Give the position of every leukocyte visible.
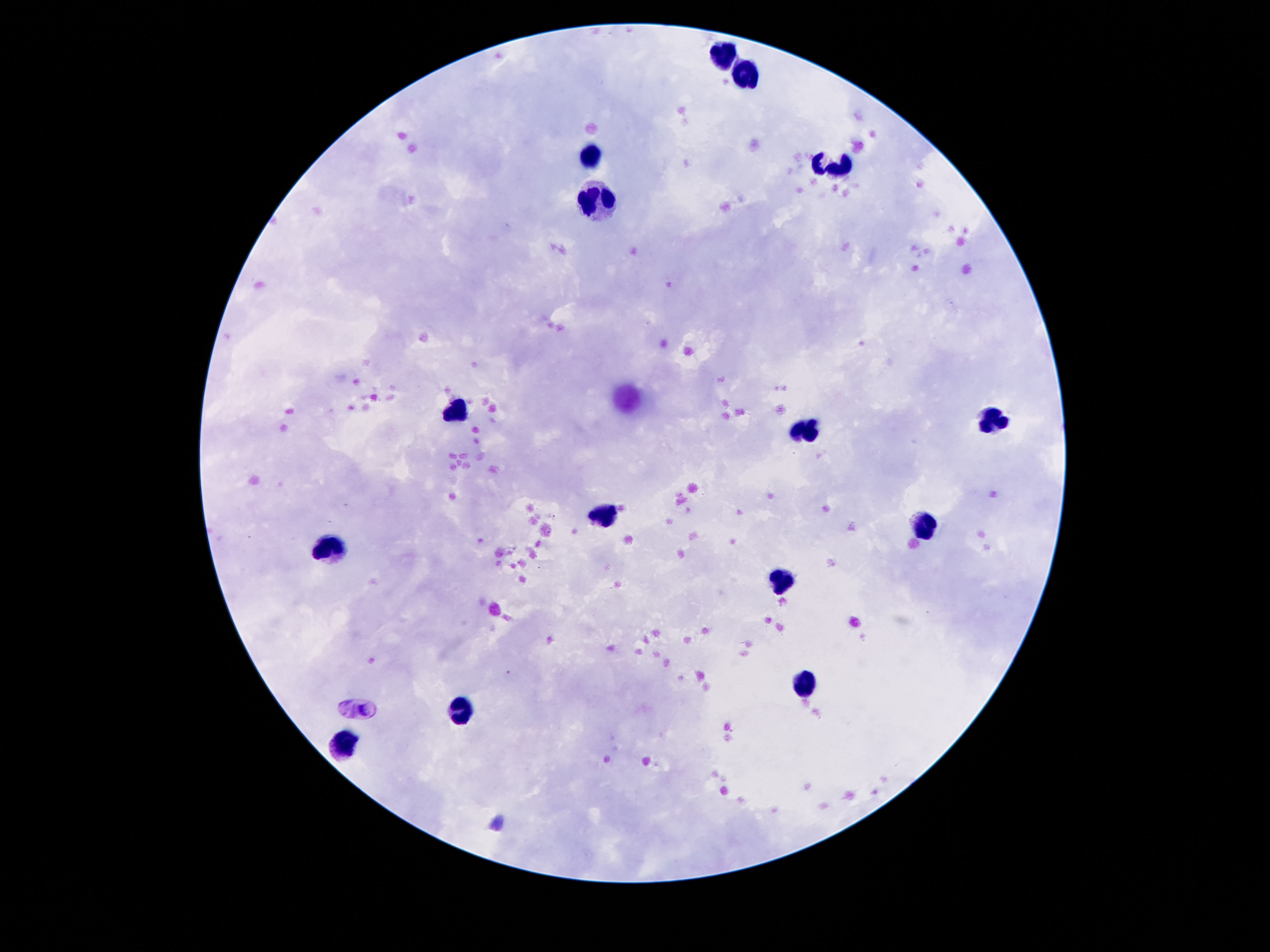

Approximate object centers, in pixels from the top-left corner.
Leukocytes: (x=721, y=56), (x=746, y=76), (x=591, y=153), (x=836, y=164), (x=593, y=203), (x=456, y=411), (x=994, y=420), (x=811, y=432), (x=605, y=516), (x=923, y=521), (x=330, y=551), (x=776, y=574), (x=807, y=685), (x=465, y=712), (x=345, y=746).

image size = 1270×952 pixels
field of view = single
capture = smartphone camera through the microscope eyepiece
preparation = thick blood film
patient malaria status = not infected
stain = Giemsa
magnification = 100x